Report the malaria status of this cell.
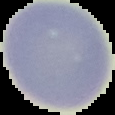
It is uninfected.

image size = 115×115 pixels
image type = segmented cell region with the area outside set to black
preparation = thin blood smear